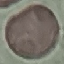
malaria status = uninfected
preparation = thin blood smear
stain = Giemsa
image type = automatically extracted cell patch, resized to 64 × 64 pixels
capture = smartphone through the microscope eyepiece